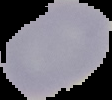
{
  "image_type": "segmented cell region on a black background",
  "preparation": "thin blood film",
  "result": "negative for malaria parasites",
  "image_size": "112×100 pixels"
}